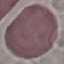
malaria_status: uninfected
image_type: automatically extracted cell patch, resized to 64 × 64 pixels
stain: Giemsa
preparation: thin blood film
capture: smartphone through the microscope eyepiece